Locate every blood parasite and identify its species.
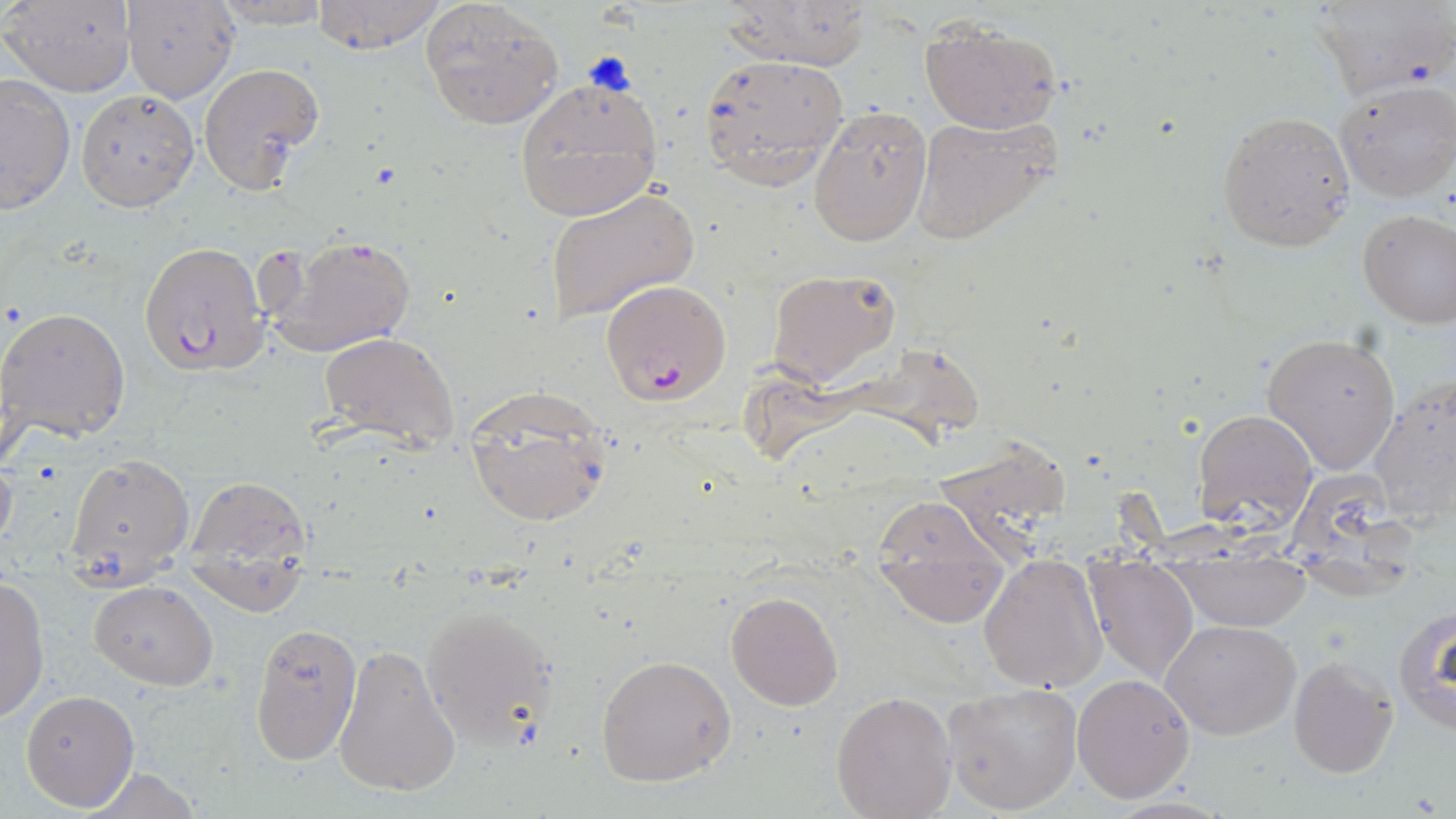
Approximate bounding boxes as (x1, y1, x2, y2) in pixels.
Plasmodium falciparum-infected red blood cells: (139, 240, 272, 377), (599, 279, 731, 407).
No Plasmodium ovale, Plasmodium malariae, Plasmodium vivax, Babesia divergens, or Trypanosoma brucei observed.

Uninfected red blood cell locations: (309, 0, 448, 55), (3, 1, 135, 97), (213, 1, 332, 28), (420, 1, 564, 129), (718, 1, 872, 72), (1310, 1, 1451, 100), (123, 2, 240, 103), (919, 18, 1063, 134), (697, 50, 850, 189), (197, 61, 325, 192), (0, 73, 75, 214), (513, 77, 663, 222), (1335, 78, 1456, 201), (74, 89, 198, 211), (807, 104, 931, 247), (1216, 109, 1356, 253), (910, 113, 1060, 246), (544, 186, 699, 326), (1358, 210, 1456, 328), (262, 233, 418, 360), (766, 268, 901, 389), (0, 307, 132, 442), (1262, 331, 1403, 474), (318, 332, 460, 451), (753, 338, 985, 469), (1366, 380, 1455, 530), (460, 386, 614, 528), (1193, 408, 1318, 530), (946, 435, 1077, 564), (0, 448, 18, 560), (65, 454, 194, 574), (1296, 470, 1412, 599), (181, 472, 318, 613), (872, 493, 1014, 627), (978, 554, 1109, 693), (1081, 557, 1200, 686), (1167, 559, 1313, 633), (0, 575, 50, 723), (89, 580, 219, 691), (725, 590, 844, 712), (420, 602, 560, 752), (1392, 609, 1456, 736), (1162, 619, 1301, 740), (248, 622, 363, 765), (333, 642, 462, 799), (595, 655, 737, 788), (1288, 656, 1398, 778), (1070, 672, 1196, 803), (942, 681, 1082, 815), (20, 690, 140, 811), (831, 691, 957, 819), (76, 765, 208, 819). Slide-level diagnosis: Plasmodium falciparum. May-Grünwald-Giemsa stain. Thin blood smear. Light microscopy. Image is 1456×819 pixels. Single field of view. 1000x magnification.